State which parasite is depicted.
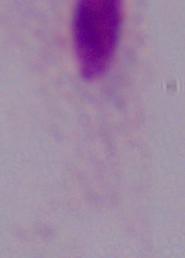
A trichomonad.

Micrograph. Captured at 1000x magnification.